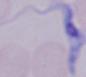

Captured at 1000x magnification. A trypanosome is shown. Micrograph.